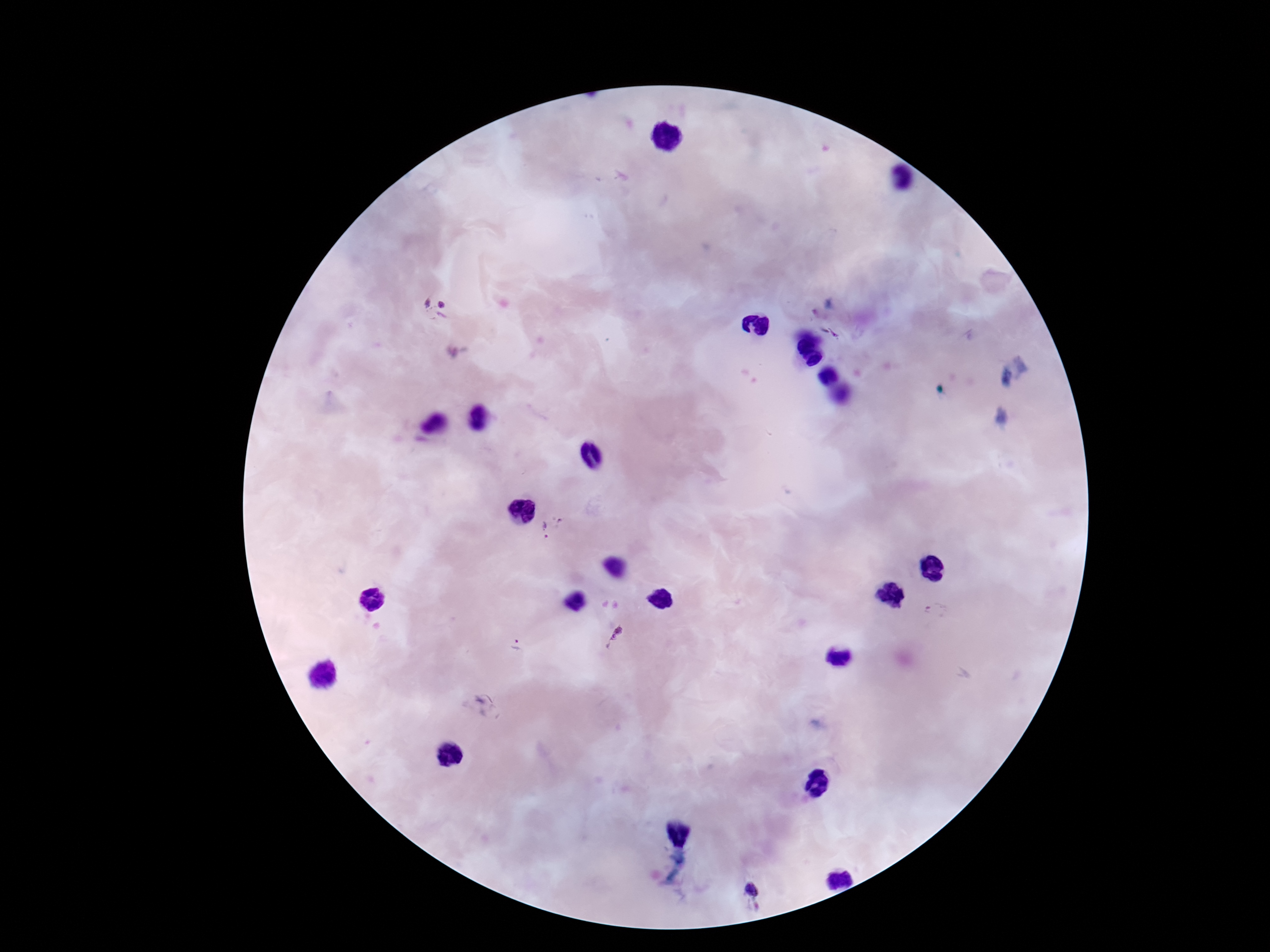

{
  "magnification": "100x",
  "plasmodium_parasite_locations": "approximate centers as [x, y] in pixels: [434, 309], [549, 530], [935, 611], [613, 637], [516, 644], [752, 892]",
  "image_size": "1270×952 pixels",
  "capture": "smartphone camera through the microscope eyepiece",
  "field_of_view": "one from this slide",
  "stain": "Giemsa",
  "patient_malaria_status": "positive",
  "preparation": "thick blood film"
}